Assess the morphology of the erythrocytes.
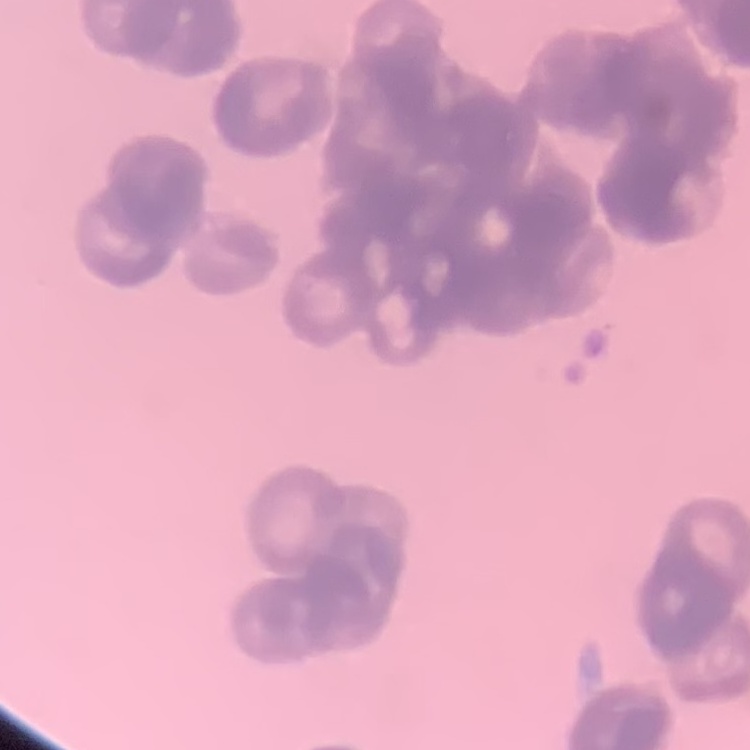

They show rouleaux formation.

One tile cut from a larger photomicrograph. Field's or Giemsa stain. Thin blood smear.